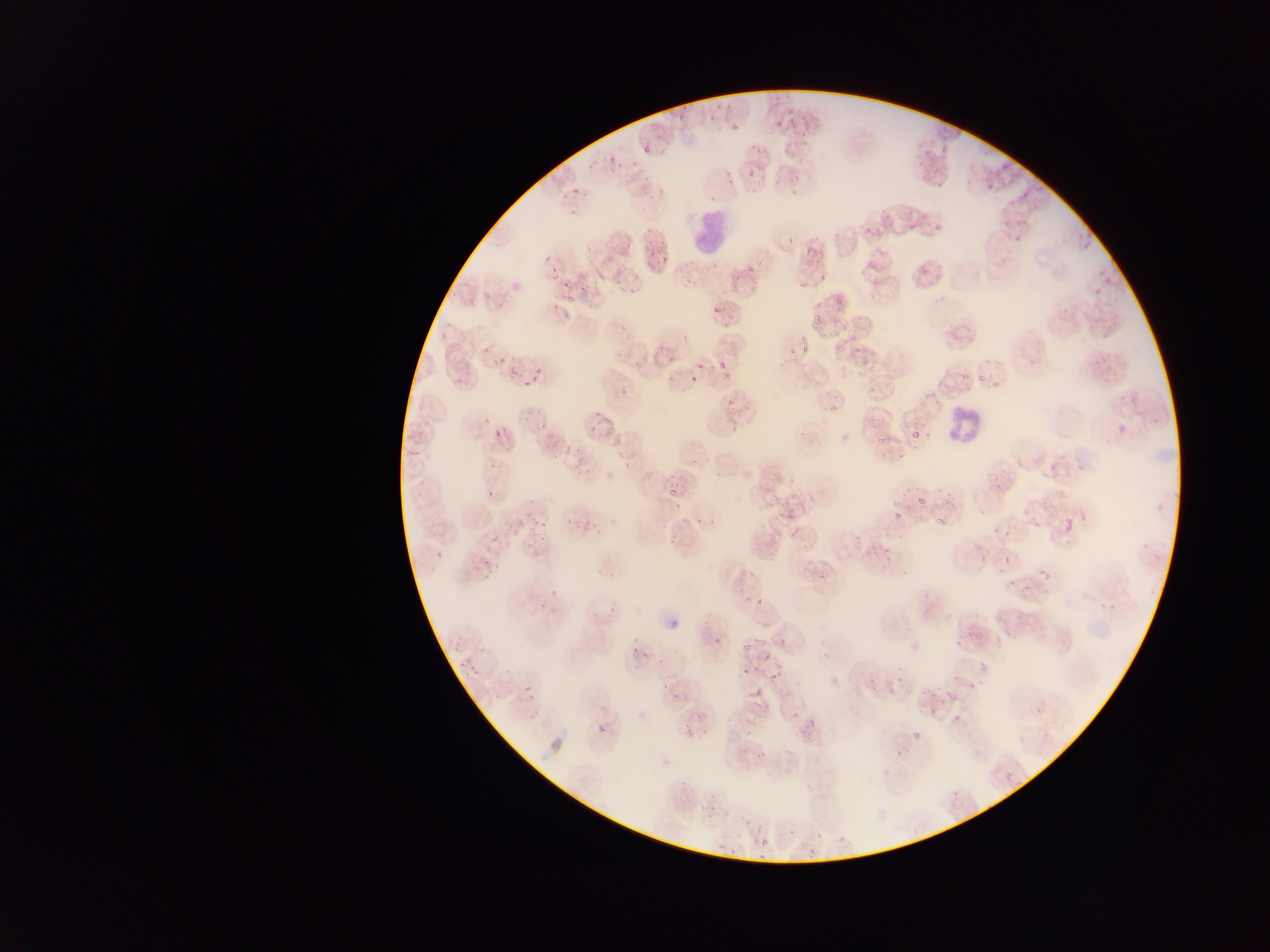 Approximate bounding boxes as {left, top, right, bottom} in pixels. Plasmodium parasite locations: {677, 100, 691, 120}, {710, 100, 720, 118}, {788, 107, 799, 124}, {774, 113, 783, 127}, {729, 115, 741, 130}, {643, 136, 656, 156}, {934, 137, 951, 153}, {754, 145, 767, 161}, {607, 149, 618, 166}, {922, 149, 928, 158}, {588, 157, 597, 168}, {626, 158, 639, 170}, {998, 162, 1016, 172}, {934, 172, 947, 186}, {748, 174, 761, 196}, {782, 174, 801, 183}, {984, 176, 998, 200}, {788, 183, 803, 201}, {571, 186, 581, 196}, {656, 188, 666, 200}, {1023, 191, 1029, 199}, {880, 209, 889, 218}, {907, 223, 916, 231}, {935, 223, 941, 232}, {862, 225, 871, 232}, {1077, 229, 1097, 251}, {1011, 232, 1024, 242}, {654, 238, 663, 254}, {802, 245, 816, 258}, {543, 250, 561, 261}, {661, 254, 669, 263}, {737, 254, 763, 279}, {711, 258, 721, 268}, {1095, 267, 1114, 282}, {547, 269, 557, 279}, {819, 270, 826, 287}, {557, 274, 571, 291}, {578, 277, 591, 290}, {505, 279, 517, 294}, {618, 280, 636, 297}, {1092, 285, 1103, 296}, {480, 286, 490, 301}, {833, 293, 846, 305}, {565, 296, 574, 304}, {465, 297, 478, 307}, {548, 297, 562, 309}, {496, 298, 508, 311}, {710, 301, 722, 312}, {809, 313, 824, 330}, {612, 314, 638, 329}, {719, 317, 735, 333}, {438, 328, 448, 338}, {965, 331, 979, 344}, {835, 341, 844, 350}, {447, 342, 458, 353}, {803, 344, 810, 353}, {492, 345, 508, 365}, {610, 345, 621, 359}, {652, 346, 661, 354}, {788, 346, 798, 355}, {664, 350, 681, 363}, {713, 356, 729, 372}, {531, 360, 541, 376}, {695, 362, 705, 373}, {507, 366, 521, 376}, {660, 368, 675, 388}, {721, 368, 738, 382}, {973, 368, 988, 384}, {455, 373, 469, 385}, {687, 377, 697, 384}, {522, 379, 534, 387}, {993, 381, 1003, 396}, {866, 382, 877, 396}, {617, 389, 631, 395}, {723, 394, 738, 407}, {824, 398, 843, 414}, {522, 408, 536, 427}, {476, 411, 496, 428}, {600, 411, 615, 425}, {729, 413, 739, 442}, {541, 419, 548, 428}, {585, 419, 598, 432}, {924, 419, 932, 443}, {1115, 421, 1126, 438}, {491, 422, 510, 436}, {908, 430, 918, 444}, {875, 431, 890, 445}, {611, 433, 625, 446}, {556, 439, 584, 456}, {894, 445, 905, 463}, {689, 453, 703, 469}, {570, 454, 592, 475}, {1046, 454, 1061, 479}, {621, 460, 633, 471}, {1073, 460, 1091, 470}, {775, 476, 785, 485}, {666, 482, 680, 496}, {936, 487, 955, 498}, {483, 488, 496, 505}, {769, 492, 777, 503}, {916, 496, 923, 510}, {777, 500, 788, 509}, {675, 504, 684, 512}, {894, 509, 902, 518}, {935, 513, 950, 529}, {590, 515, 598, 530}, {708, 515, 716, 524}, {1063, 516, 1075, 538}, {528, 518, 539, 527}, {1032, 518, 1042, 528}, {695, 519, 701, 528}, {573, 521, 585, 537}, {543, 522, 554, 530}, {1000, 525, 1014, 537}, {524, 530, 538, 550}, {490, 531, 506, 546}, {786, 531, 795, 540}, {666, 537, 678, 548}, {873, 544, 895, 562}, {436, 547, 446, 560}, {977, 547, 990, 562}, {1004, 548, 1013, 562}, {476, 558, 497, 576}, {1035, 561, 1052, 582}, {997, 564, 1008, 579}, {1004, 575, 1020, 591}, {547, 586, 563, 603}, {753, 596, 768, 607}, {1098, 597, 1119, 614}, {539, 598, 548, 614}, {609, 605, 618, 616}, {591, 610, 599, 621}, {703, 615, 712, 628}, {451, 631, 463, 652}, {713, 631, 724, 647}, {954, 631, 968, 649}, {629, 632, 640, 657}, {755, 635, 767, 646}, {740, 644, 753, 653}, {641, 650, 652, 659}, {766, 650, 775, 659}, {465, 661, 477, 673}, {740, 667, 753, 676}, {897, 674, 906, 691}, {969, 674, 982, 691}, {764, 676, 782, 684}, {905, 681, 913, 695}, {523, 684, 535, 695}, {667, 685, 683, 702}, {750, 685, 763, 697}, {885, 687, 895, 696}, {947, 694, 959, 705}, {1034, 705, 1044, 716}, {927, 706, 940, 722}, {952, 709, 962, 723}, {598, 723, 607, 736}, {911, 734, 924, 744}, {1004, 773, 1013, 783}, {759, 838, 770, 847} | approximate {x, y} pixel centers of objects too small to bound: {567, 521}. Leukocyte locations: {696, 207, 722, 252}, {943, 396, 984, 454}. Collected in Ghana. Image is 1270×952 pixels. One field of view. Photographed through a microscope with a mobile-phone camera. Thin blood smear.